Outline platelets.
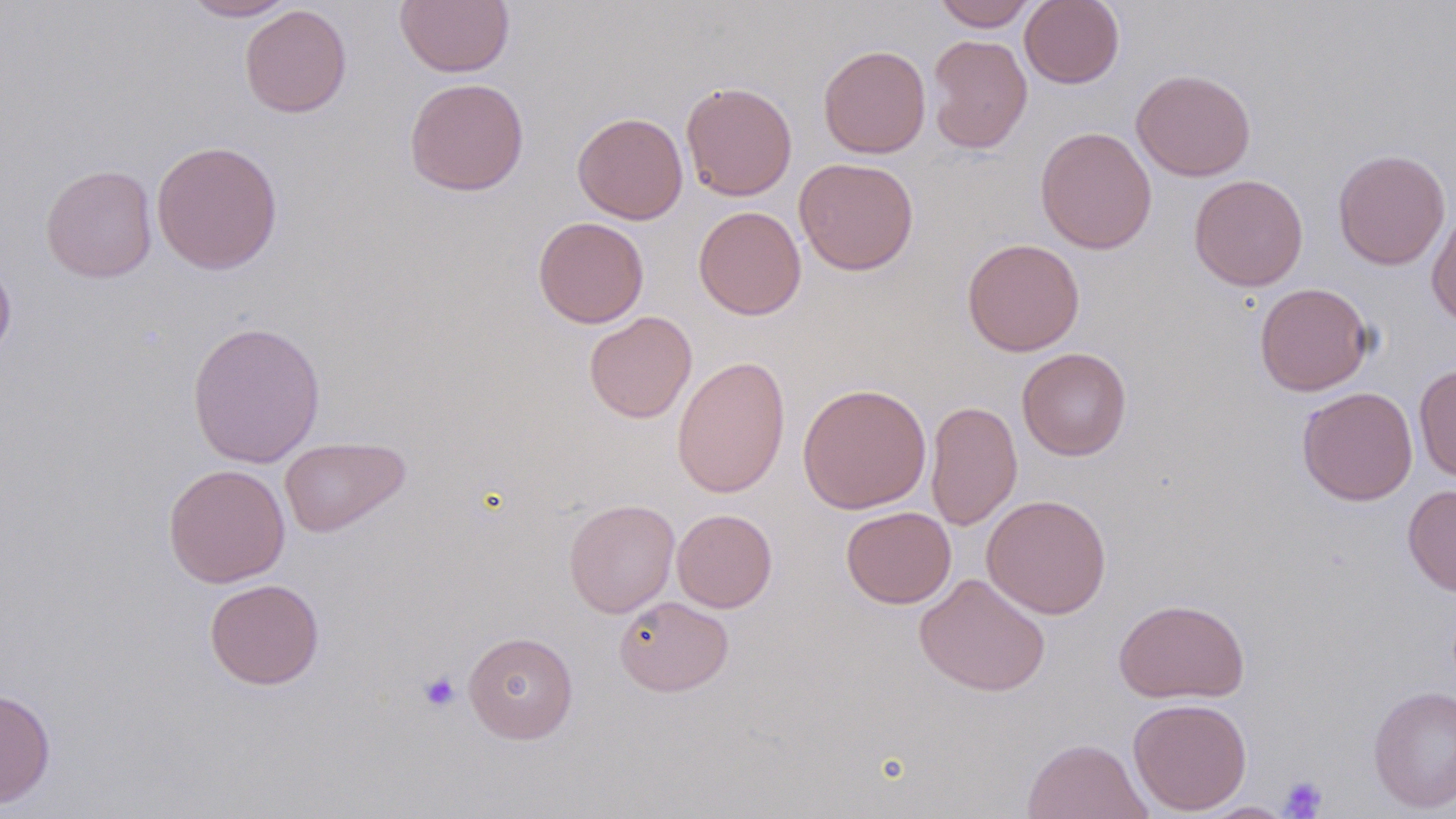
Approximate bounding boxes as (x1, y1, x2, y2) in pixels.
Platelets: (419, 670, 461, 712), (1280, 776, 1328, 817).

slide-level diagnosis = negative for blood parasites
stain = May-Grünwald-Giemsa
image size = 1456×819 pixels
magnification = 1000x
modality = optical microscopy
field of view = one of a larger specimen
uninfected red blood cell locations = approximate bounding boxes as (x1, y1, x2, y2) in pixels: (182, 0, 300, 21), (395, 0, 514, 77), (932, 0, 1036, 31), (1020, 0, 1125, 89), (240, 4, 352, 117), (927, 34, 1032, 153), (818, 44, 931, 159), (1131, 68, 1257, 181), (404, 77, 529, 196), (680, 81, 797, 201), (572, 111, 688, 224), (1035, 126, 1156, 254), (151, 140, 283, 274), (1333, 149, 1451, 270), (793, 157, 919, 276), (41, 164, 157, 283), (1189, 174, 1308, 291), (693, 206, 806, 320), (1426, 207, 1456, 326), (533, 216, 649, 328), (962, 238, 1084, 356), (0, 257, 16, 363), (1254, 282, 1374, 396), (584, 311, 697, 423), (186, 319, 326, 468), (1017, 347, 1131, 461), (672, 355, 791, 498), (1414, 362, 1456, 484), (797, 382, 931, 514), (1297, 386, 1418, 506), (925, 399, 1022, 532), (279, 436, 410, 538), (163, 464, 291, 587), (1403, 484, 1456, 597), (981, 494, 1111, 619), (564, 498, 680, 618), (841, 506, 956, 608), (672, 508, 777, 613), (914, 573, 1051, 697), (204, 578, 325, 690), (613, 596, 733, 696), (1114, 598, 1249, 703), (463, 631, 578, 743), (1368, 685, 1456, 814), (0, 687, 56, 808), (1127, 697, 1252, 815), (1020, 737, 1153, 819), (1198, 801, 1296, 818)
preparation = thin blood film